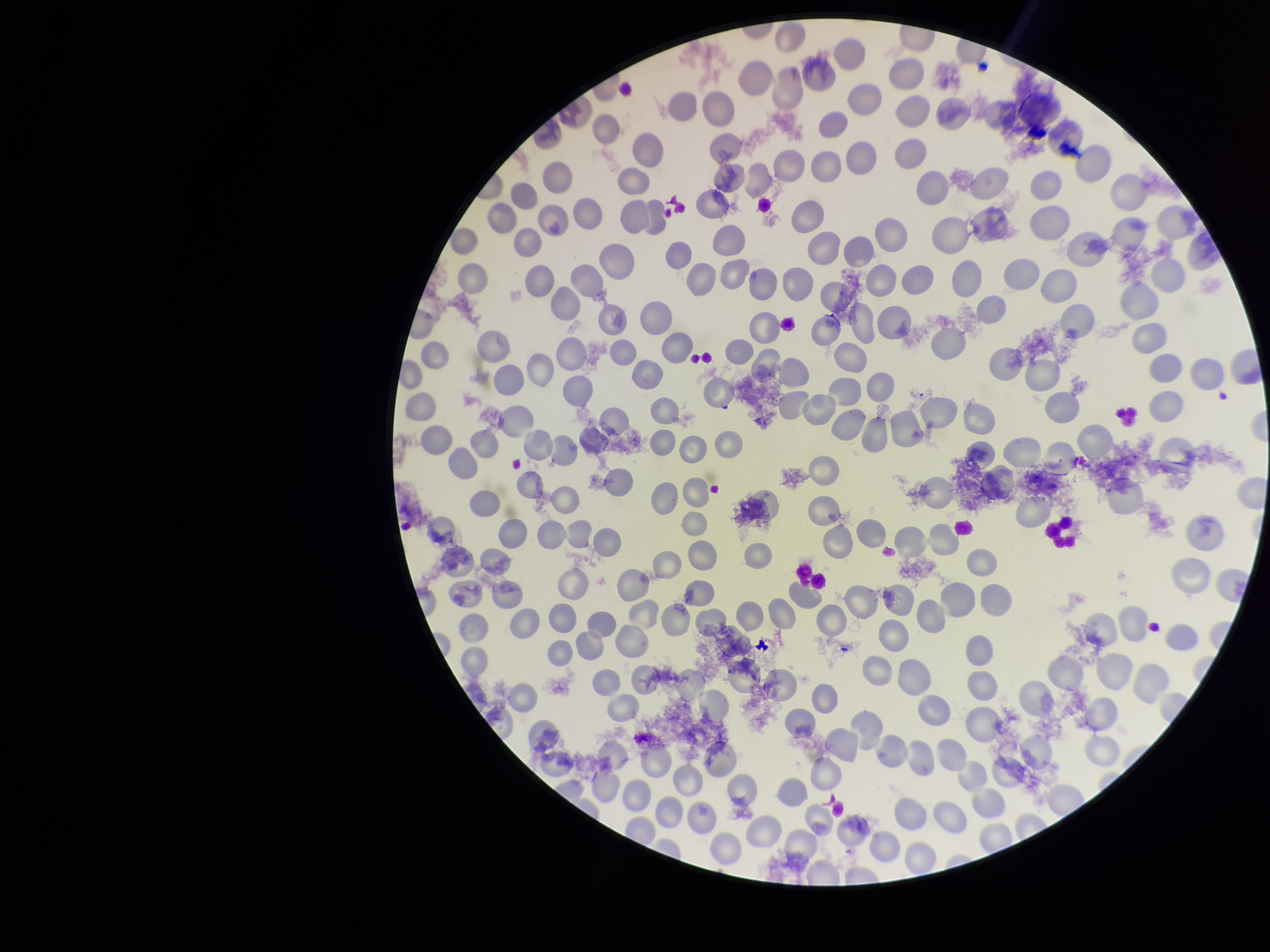

Species reported for this patient: Plasmodium falciparum. Smartphone photograph taken through the eyepiece of a microscope. Stained with Giemsa. Single field of view. Patient malaria status: positive. Parasitized red blood cell count: 0. Parasitized red blood cells: none seen. Preparation: thin blood smear. Red blood cell count: 244. Image is 1270×952 pixels.